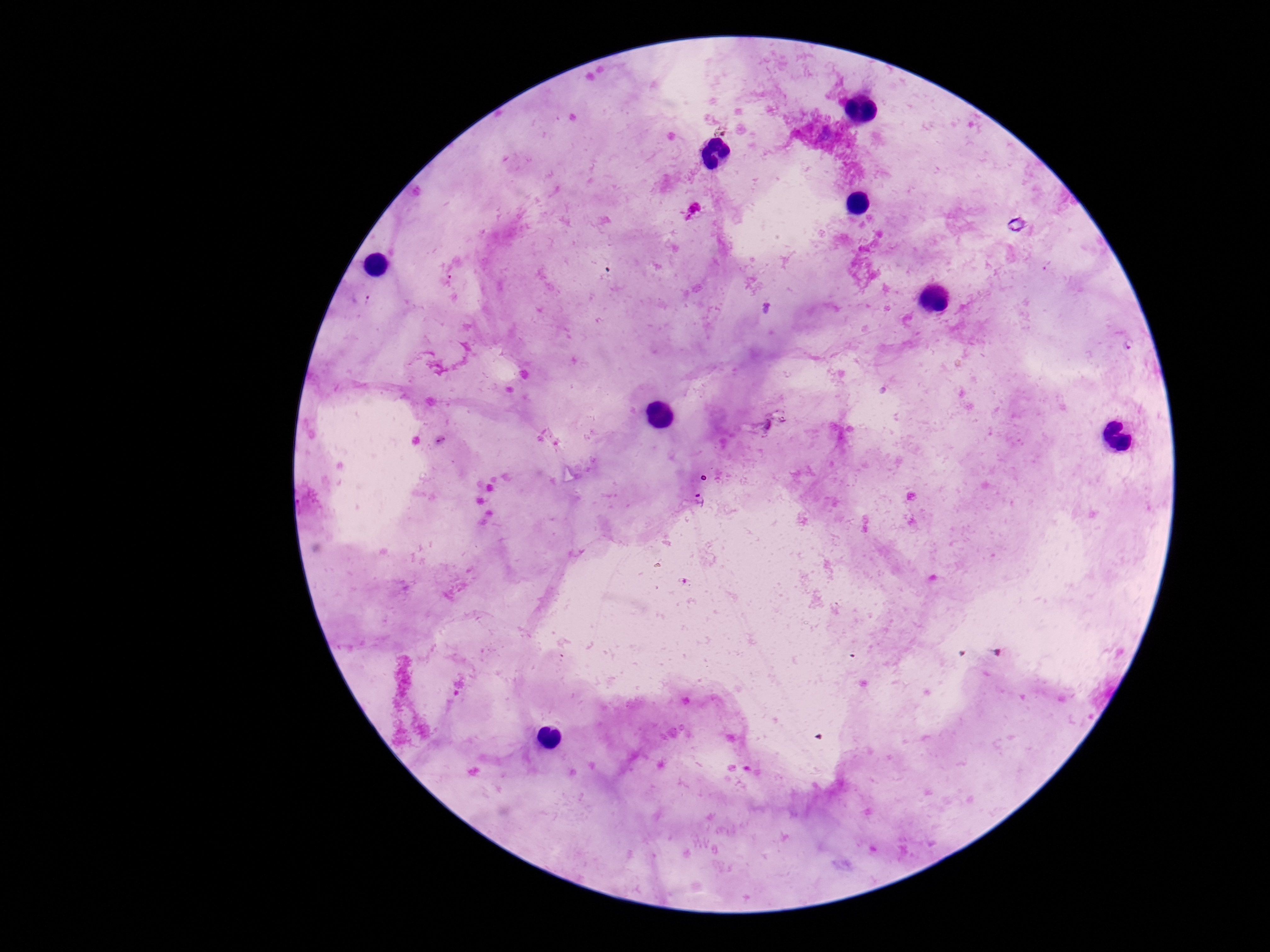

Approximate centers as (x, y) in pixels. Plasmodium parasite locations: (449, 280), (363, 297), (765, 309), (1130, 345), (768, 424), (700, 499). Image is 1270×952 pixels. One field from this slide. Giemsa stain. Smartphone photograph taken through the microscope eyepiece. Patient malaria status: infected. Thick blood smear. 100x magnification.